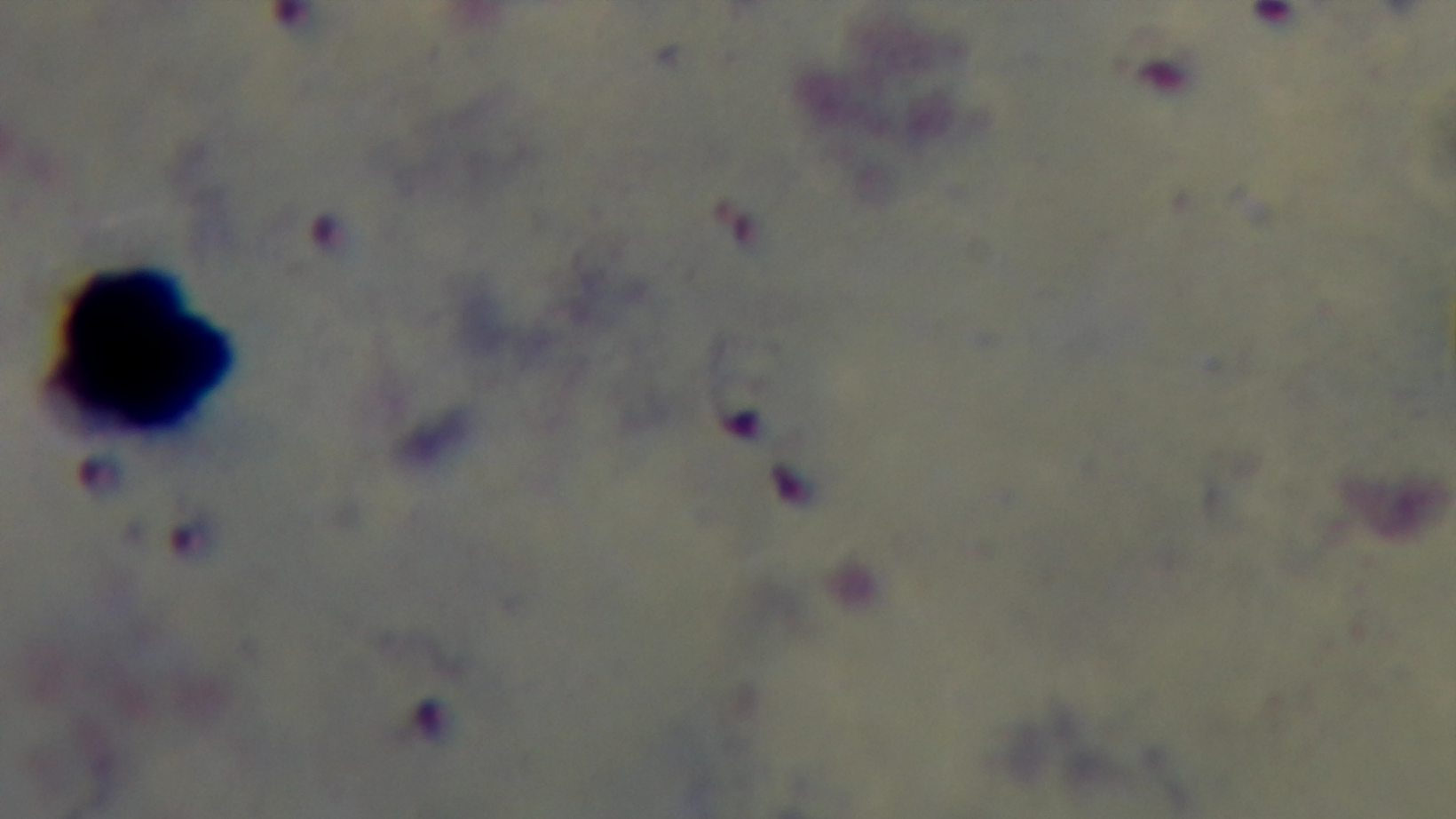
{
  "modality": "light microscopy",
  "field_of_view": "one from the slide",
  "objective": "100x oil immersion",
  "stain": "Giemsa",
  "preparation": "thick smear",
  "capture": "mounted 4K digital camera",
  "malaria_status": "positive"
}